Give the extent of all Plasmodium malariae-infected red blood cells.
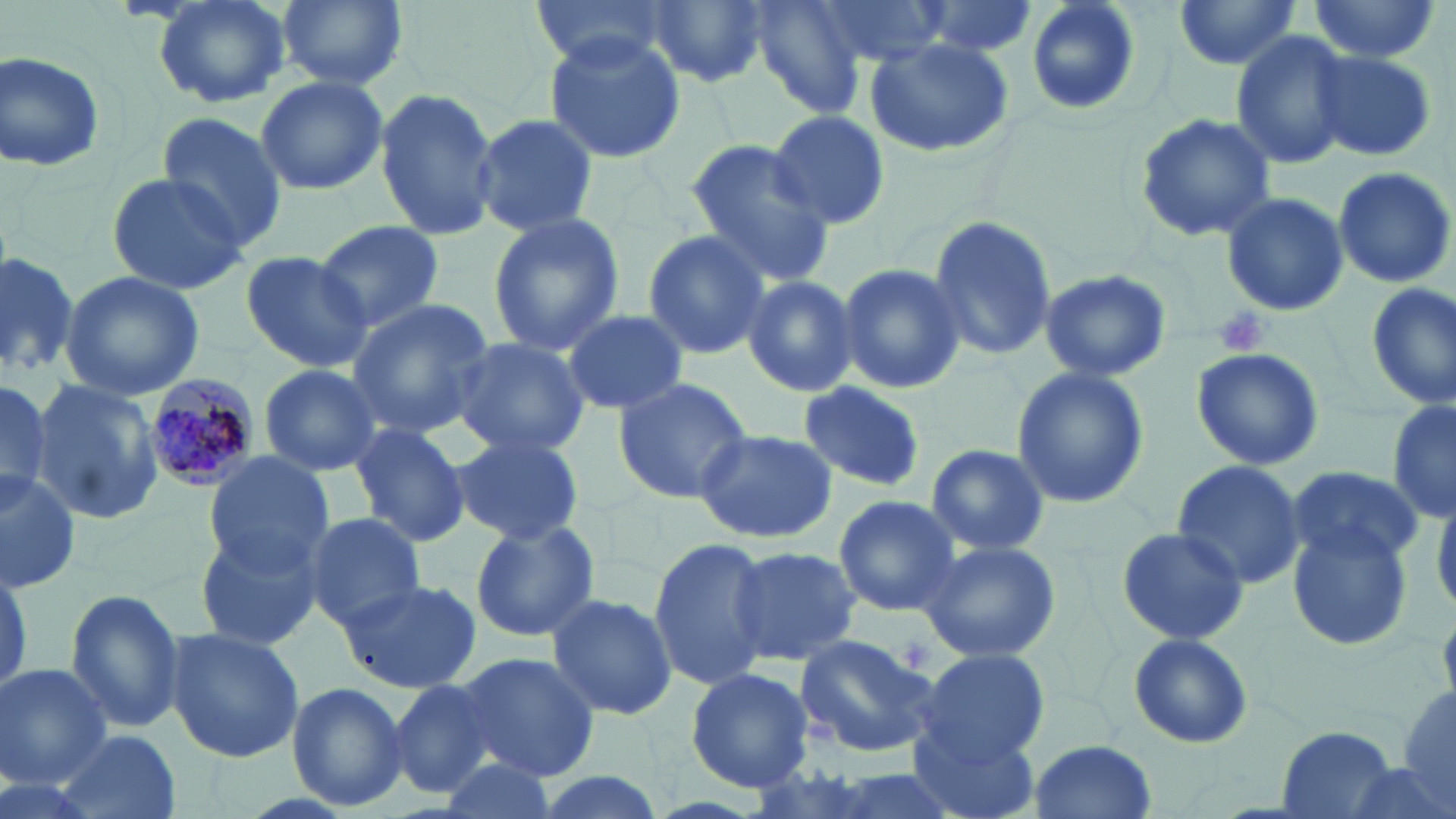

Approximate bounding boxes as [x1, y1, x2, y2] in pixels.
Plasmodium malariae-infected red blood cells: [140, 375, 266, 493].

{
  "slide_level_diagnosis": "Plasmodium malariae",
  "stain": "May-Grünwald-Giemsa",
  "preparation": "thin blood film",
  "field_of_view": "one of a larger specimen",
  "modality": "light microscopy",
  "platelet_locations": "approximate bounding boxes as [x1, y1, x2, y2] in pixels: [1214, 304, 1270, 357]",
  "image_size": "1456×819 pixels",
  "uninfected_red_blood_cell_locations": "approximate bounding boxes as [x1, y1, x2, y2] in pixels: [152, 0, 292, 110], [274, 0, 408, 91], [531, 0, 672, 68], [641, 0, 771, 89], [745, 0, 869, 118], [803, 0, 953, 69], [904, 0, 1044, 58], [1172, 0, 1304, 71], [1305, 0, 1441, 63], [1024, 1, 1142, 115], [1229, 29, 1355, 171], [542, 30, 686, 165], [863, 34, 1014, 159], [1, 48, 107, 174], [1310, 49, 1437, 161], [254, 74, 388, 195], [374, 86, 500, 240], [766, 109, 889, 231], [1133, 112, 1277, 243], [156, 114, 290, 253], [471, 114, 599, 239], [683, 140, 835, 285], [1331, 167, 1455, 287], [106, 169, 249, 294], [1219, 191, 1350, 318], [485, 212, 625, 357], [927, 215, 1058, 362], [316, 219, 445, 334], [641, 229, 773, 359], [238, 250, 374, 375], [0, 251, 80, 379], [835, 263, 966, 395], [1039, 269, 1172, 384], [61, 272, 203, 400], [739, 273, 858, 397], [1364, 281, 1456, 413], [346, 299, 497, 435], [562, 308, 688, 414], [451, 336, 592, 460], [1191, 347, 1324, 471], [259, 363, 383, 477], [1010, 366, 1149, 509], [0, 373, 52, 506], [610, 376, 753, 504], [29, 378, 162, 527], [799, 382, 927, 492], [1387, 395, 1455, 525], [346, 423, 471, 548], [694, 428, 839, 542], [450, 436, 585, 543], [923, 442, 1051, 557], [201, 451, 334, 575], [1169, 459, 1307, 589], [1284, 466, 1426, 568], [0, 469, 81, 592], [1433, 487, 1456, 615], [834, 494, 961, 617], [304, 512, 427, 630], [468, 516, 603, 642], [1285, 521, 1416, 654], [193, 522, 330, 651], [1114, 525, 1250, 645], [917, 537, 1062, 663], [648, 538, 774, 691], [727, 543, 861, 667], [335, 578, 481, 694], [64, 588, 188, 734], [546, 592, 677, 720], [163, 626, 304, 762], [1127, 632, 1254, 749], [793, 633, 941, 758], [917, 649, 1050, 763], [457, 652, 599, 782], [0, 664, 112, 788], [685, 664, 815, 794], [390, 678, 499, 799], [286, 681, 409, 811], [1396, 686, 1456, 812], [908, 718, 1043, 819], [1277, 727, 1395, 817], [54, 729, 181, 819], [1028, 739, 1158, 819], [435, 755, 559, 818], [523, 770, 668, 819]",
  "magnification": "1000x"
}